Classify this cell by malaria status.
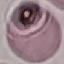
Uninfected.

Summary:
  - Preparation: thin blood film
  - Stain: Giemsa
  - Image type: cell patch, automatically extracted from a larger field of view and resized to 64 × 64 pixels
  - Capture: smartphone through the microscope eyepiece